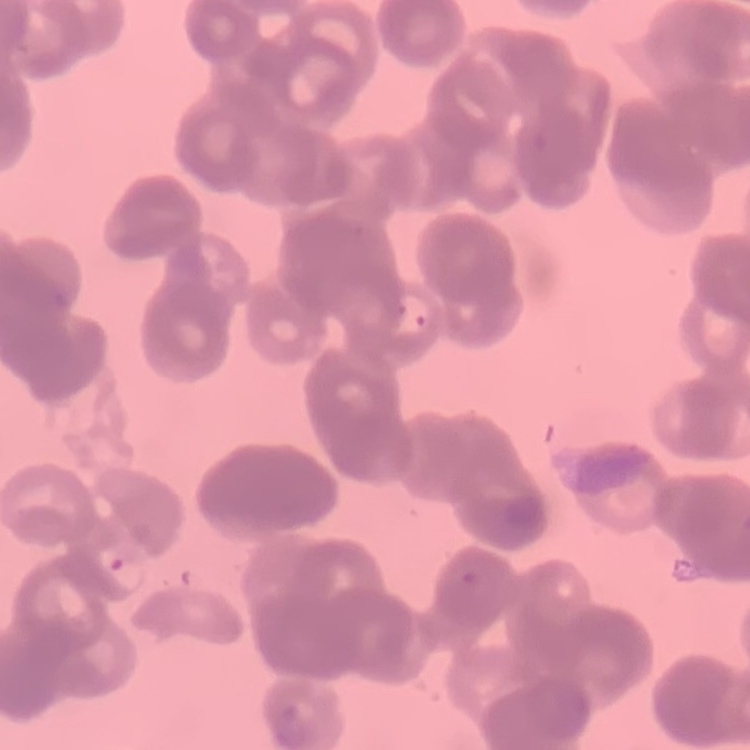
Summary:
  - Erythrocyte morphology: rouleaux formation
  - Image type: one tile cut from a larger photomicrograph
  - Preparation: thin blood film
  - Stain: Field's or Giemsa